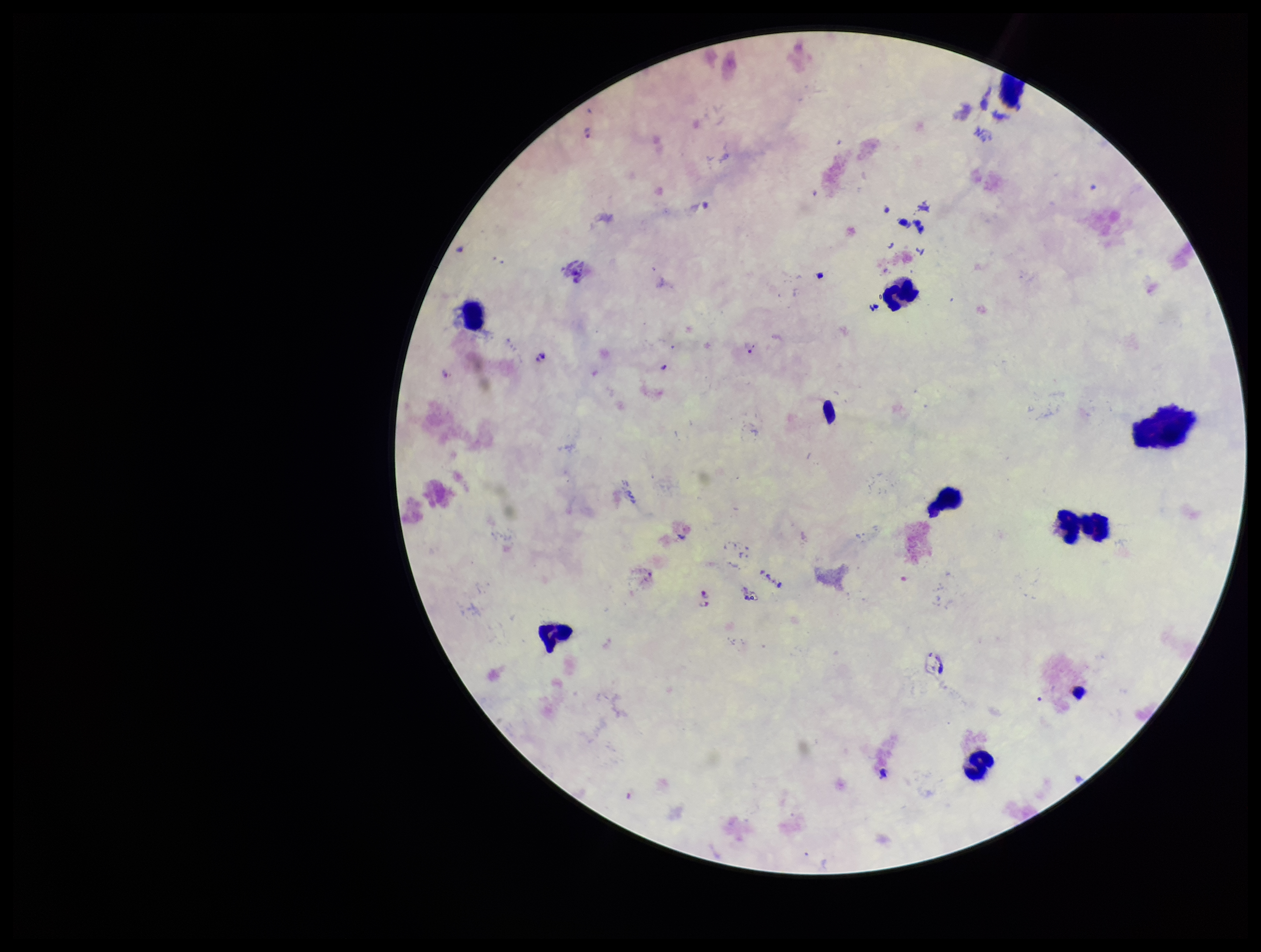
preparation = thick blood smear
species reported for this patient = Plasmodium falciparum
stain = Giemsa
image size = 1261×952 pixels
capture = smartphone photograph through the microscope eyepiece
field of view = single
Plasmodium parasites = seen
parasite count = 8
leukocyte count = 8
patient malaria status = infected